Report the malaria status of this cell.
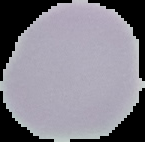
Uninfected.

From a thin blood film. Image is 145×142 pixels. The area outside the segmented cell region is set to black.